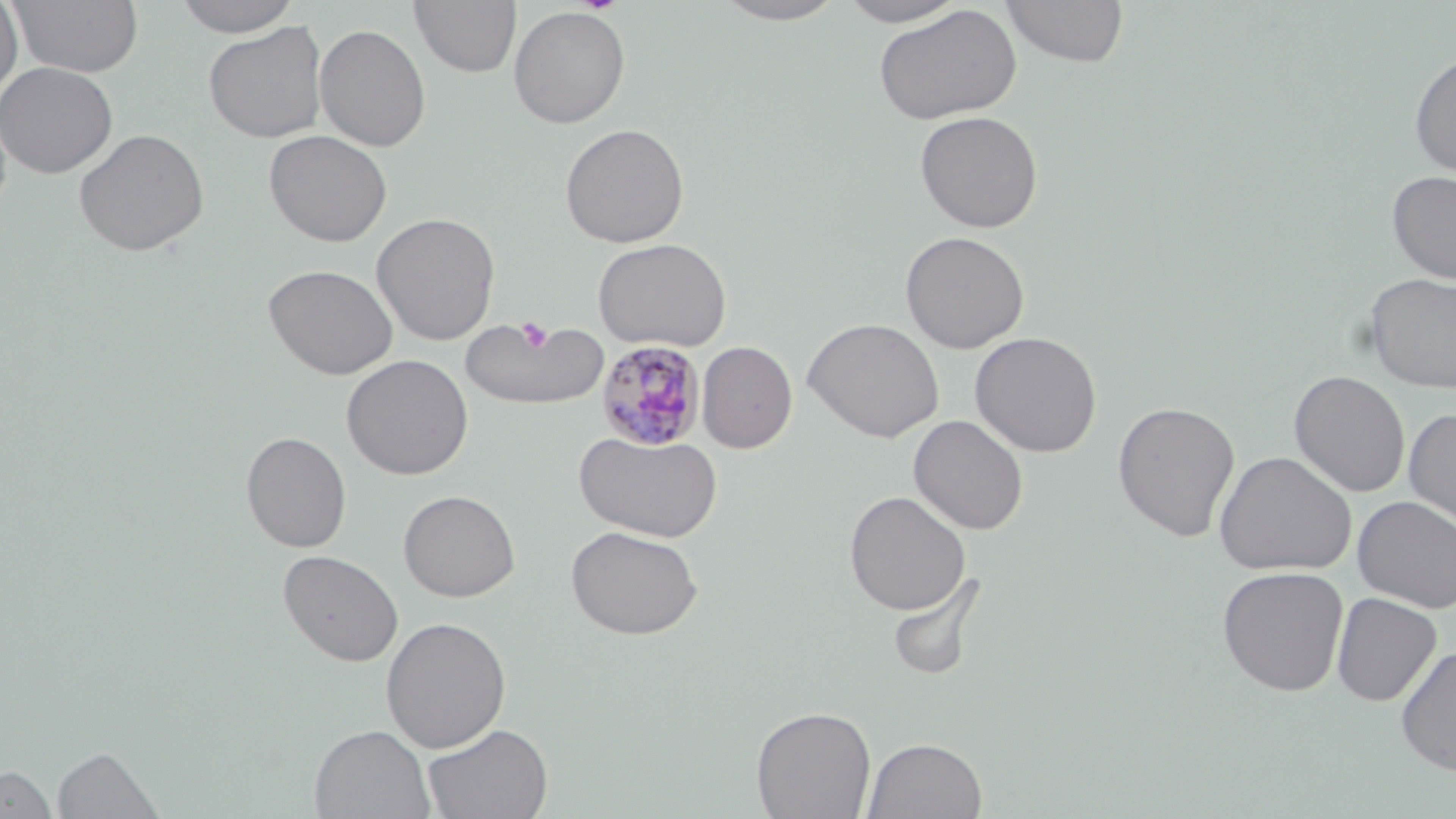

Summary:
  - Coordinate format: approximate bounding boxes as (x1,y1)-(x2,y2) corner pairs in pixels
  - Plasmodium malariae-infected red blood cell locations: (597,341)-(706,451)
  - Platelet locations: (516,316)-(554,356)
  - Uninfected red blood cell locations: (0,0)-(23,102), (172,0)-(302,37), (409,0)-(521,78), (710,0)-(851,25), (835,0)-(970,27), (1002,0)-(1129,68), (7,1)-(144,78), (873,4)-(1022,125), (508,6)-(630,128), (203,21)-(328,143), (313,23)-(431,152), (1409,50)-(1456,179), (0,61)-(118,179), (914,110)-(1043,233), (559,123)-(689,248), (73,128)-(210,257), (263,129)-(392,247), (1387,170)-(1456,284), (371,212)-(500,345), (900,231)-(1029,353), (592,238)-(732,351), (263,263)-(398,380), (1365,273)-(1456,393), (460,315)-(609,412), (803,317)-(945,442), (970,331)-(1102,457), (697,342)-(797,453), (342,354)-(473,480), (1288,369)-(1411,497), (1112,401)-(1241,542), (1403,408)-(1456,532), (908,415)-(1029,534), (573,430)-(723,542), (240,431)-(352,553), (1214,450)-(1357,576), (398,489)-(520,602), (844,490)-(971,615), (1352,495)-(1456,613), (566,525)-(703,640), (278,549)-(403,667), (1216,566)-(1349,696), (886,569)-(988,682), (1331,592)-(1442,706), (380,616)-(512,752), (1395,646)-(1456,777), (750,705)-(877,819), (421,722)-(553,819), (309,724)-(436,819), (862,736)-(988,819), (53,745)-(165,819), (0,764)-(56,818)
  - Slide-level diagnosis: Plasmodium malariae
  - Modality: optical microscopy
  - Field of view: one of a larger specimen
  - Image size: 1456×819 pixels
  - Stain: May-Grünwald-Giemsa
  - Magnification: 1000x
  - Preparation: thin blood film